Name the cell type shown.
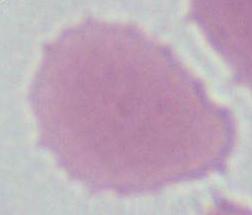

An erythrocyte.

Photomicrograph. 1000x magnification.